Identify the blood parasite species.
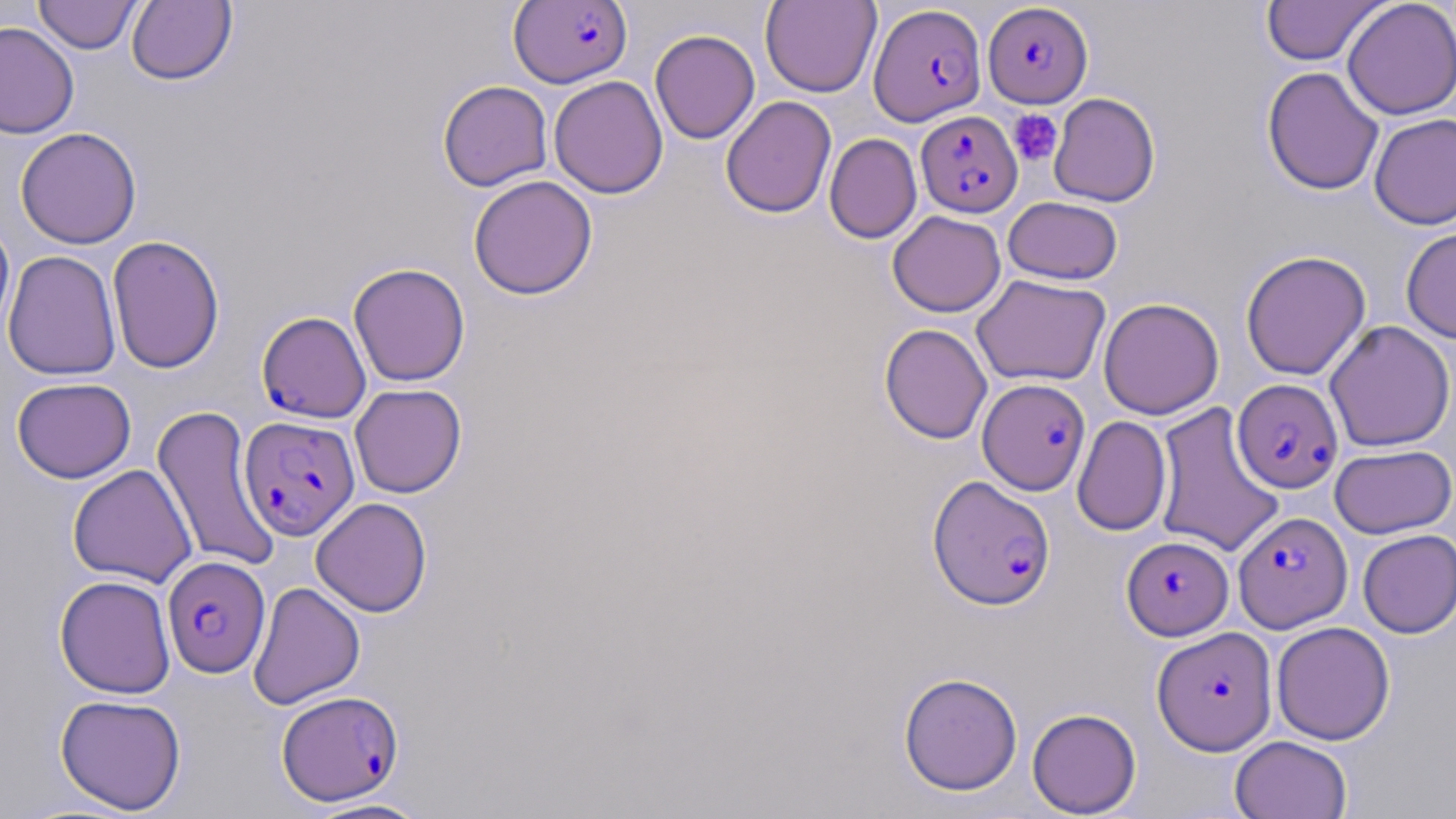
Plasmodium falciparum.

Summary:
  - Coordinate format: approximate bounding boxes as (x1, y1, x2, y2) in pixels
  - Plasmodium falciparum-infected red blood cell locations: (508, 1, 633, 88), (983, 3, 1093, 107), (868, 4, 986, 126), (916, 110, 1022, 217), (257, 311, 371, 422), (1232, 378, 1343, 493), (977, 379, 1090, 495), (239, 415, 360, 540), (928, 475, 1056, 610), (1234, 512, 1352, 632), (1122, 536, 1233, 640), (162, 555, 271, 678), (1152, 626, 1277, 755), (276, 690, 403, 806)
  - Uninfected red blood cell locations: (34, 0, 141, 54), (126, 0, 237, 86), (760, 0, 882, 97), (1261, 0, 1386, 66), (1342, 0, 1456, 120), (0, 21, 80, 138), (650, 29, 760, 144), (1261, 66, 1384, 195), (549, 75, 668, 199), (437, 80, 553, 191), (1048, 92, 1160, 207), (720, 96, 837, 218), (1369, 112, 1456, 230), (15, 127, 142, 249), (824, 133, 922, 243), (468, 175, 598, 300), (1003, 197, 1123, 285), (887, 210, 1006, 317), (0, 217, 15, 343), (1401, 227, 1456, 344), (106, 235, 225, 374), (2, 250, 121, 381), (1240, 250, 1371, 380), (348, 262, 470, 387), (971, 273, 1110, 387), (1098, 297, 1223, 419), (1324, 320, 1455, 452), (879, 323, 993, 444), (12, 377, 136, 483), (350, 383, 467, 498), (1152, 401, 1285, 559), (151, 404, 281, 572), (1072, 415, 1172, 536), (1330, 444, 1455, 538), (67, 464, 197, 588), (310, 497, 432, 617), (1357, 529, 1456, 638), (54, 575, 176, 699), (248, 581, 366, 710), (1271, 621, 1395, 745), (898, 672, 1023, 796), (55, 694, 187, 814), (1027, 708, 1142, 817), (1230, 735, 1353, 819), (304, 797, 435, 818)
  - Platelet locations: (1008, 109, 1063, 167)
  - Preparation: thin blood smear
  - Stain: May-Grünwald-Giemsa
  - Field of view: single
  - Image size: 1456×819 pixels
  - Magnification: 1000x
  - Modality: light microscopy